Classify this cell by malaria status.
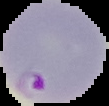
It is parasitized.

From a thin blood smear. Cell region segmented out of the field of view; the surrounding area is masked to black. Image is 109×106 pixels.